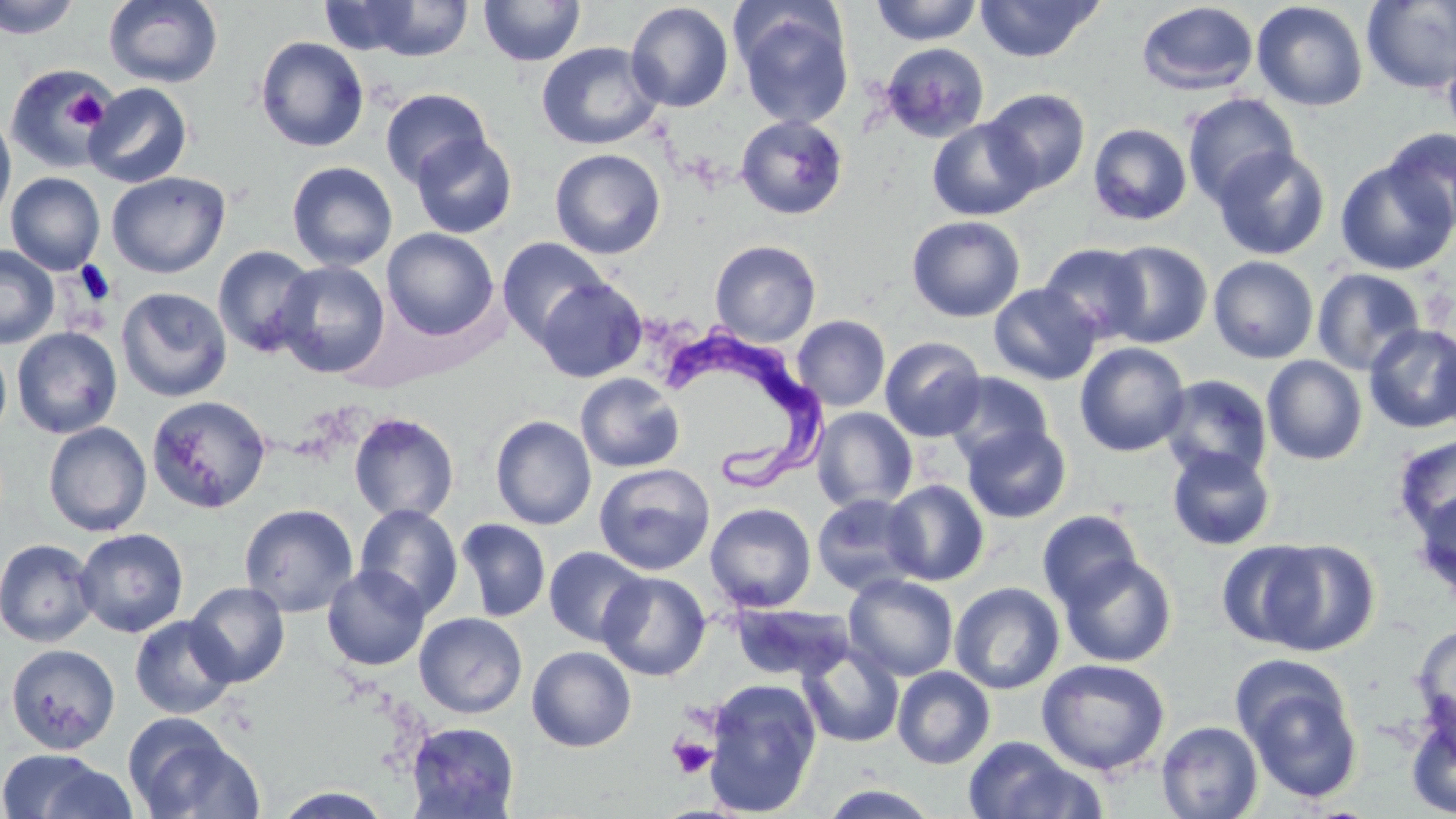

Approximate bounding boxes as (x1, y1, x2, y2) in pixels. Uninfected red blood cell locations: (0, 0, 82, 39), (103, 0, 223, 88), (478, 0, 586, 67), (870, 0, 982, 45), (975, 0, 1103, 62), (318, 1, 425, 56), (352, 1, 475, 61), (1252, 1, 1368, 112), (1362, 1, 1456, 94), (625, 2, 734, 112), (1137, 2, 1259, 96), (732, 3, 855, 130), (255, 36, 370, 152), (536, 42, 663, 150), (882, 42, 989, 143), (1442, 46, 1456, 146), (3, 64, 113, 175), (83, 82, 193, 188), (380, 88, 492, 190), (982, 88, 1090, 195), (1181, 93, 1300, 207), (0, 111, 16, 227), (735, 114, 848, 221), (927, 118, 1040, 221), (1087, 123, 1193, 226), (1384, 127, 1456, 234), (409, 132, 517, 238), (1212, 146, 1330, 260), (550, 148, 666, 259), (1335, 158, 1455, 275), (286, 161, 398, 270), (106, 171, 230, 278), (5, 172, 105, 275), (906, 215, 1026, 322), (382, 228, 499, 341), (496, 237, 612, 348), (710, 240, 821, 347), (1101, 240, 1213, 348), (1038, 243, 1151, 344), (212, 244, 318, 358), (0, 245, 59, 349), (1208, 256, 1319, 364), (274, 260, 390, 379), (1311, 267, 1426, 376), (534, 276, 647, 383), (988, 283, 1101, 385), (116, 287, 232, 402), (792, 315, 891, 412), (1364, 323, 1455, 433), (11, 327, 122, 438), (1433, 329, 1456, 434), (880, 336, 986, 442), (0, 342, 12, 441), (1075, 343, 1191, 456), (1262, 355, 1367, 465), (575, 372, 685, 473), (945, 372, 1055, 469), (1159, 375, 1273, 483), (147, 394, 272, 513), (811, 407, 917, 512), (348, 412, 459, 523), (490, 415, 596, 530), (43, 422, 151, 536), (962, 422, 1071, 523), (1392, 434, 1456, 541), (1167, 446, 1276, 550), (593, 463, 714, 575), (883, 480, 989, 585), (1411, 489, 1456, 603), (812, 493, 924, 596), (239, 503, 359, 617), (354, 503, 464, 617), (705, 503, 816, 613), (1037, 509, 1143, 610), (455, 518, 551, 622), (74, 528, 189, 638), (0, 538, 98, 647), (1257, 539, 1380, 656), (1216, 540, 1326, 650), (544, 546, 648, 646), (1059, 554, 1177, 667), (322, 564, 430, 671), (597, 570, 712, 681), (844, 573, 959, 681), (949, 581, 1065, 694), (185, 582, 289, 687), (730, 603, 853, 682), (414, 612, 528, 718), (129, 615, 238, 719), (1412, 623, 1456, 739), (5, 643, 120, 754), (527, 645, 636, 751), (798, 645, 904, 747), (1036, 658, 1170, 775), (892, 666, 996, 769), (1239, 672, 1365, 804), (703, 678, 822, 817), (1405, 703, 1456, 818), (124, 716, 262, 819), (407, 721, 519, 818), (1156, 721, 1264, 819), (961, 736, 1100, 819), (0, 749, 120, 818), (818, 784, 943, 818), (273, 786, 394, 818). Trypanosoma brucei locations: (661, 325, 835, 493). Platelet locations: (65, 89, 107, 132), (668, 736, 718, 779). Slide-level diagnosis: Trypanosoma brucei. Optical microscopy. Single field of view. Image is 1456×819 pixels. May-Grünwald-Giemsa-stained preparation. 1000x magnification. Thin blood smear.